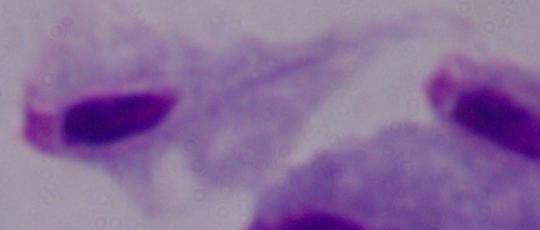
Micrograph. Captured at 1000x magnification. A trichomonad is shown.